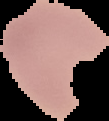

preparation = thin blood film
malaria status = uninfected
image size = 109×121 pixels
image type = segmented cell region with the area outside set to black